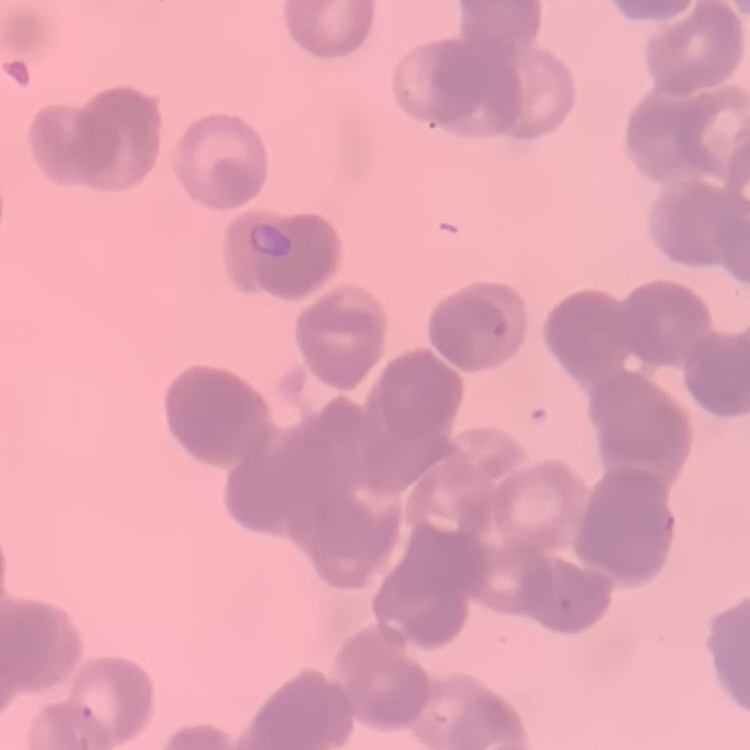
The erythrocytes show rouleaux formation. Thin peripheral smear. One tile cut from a larger photomicrograph. Stained with either Field's or Giemsa.